Report the malaria status.
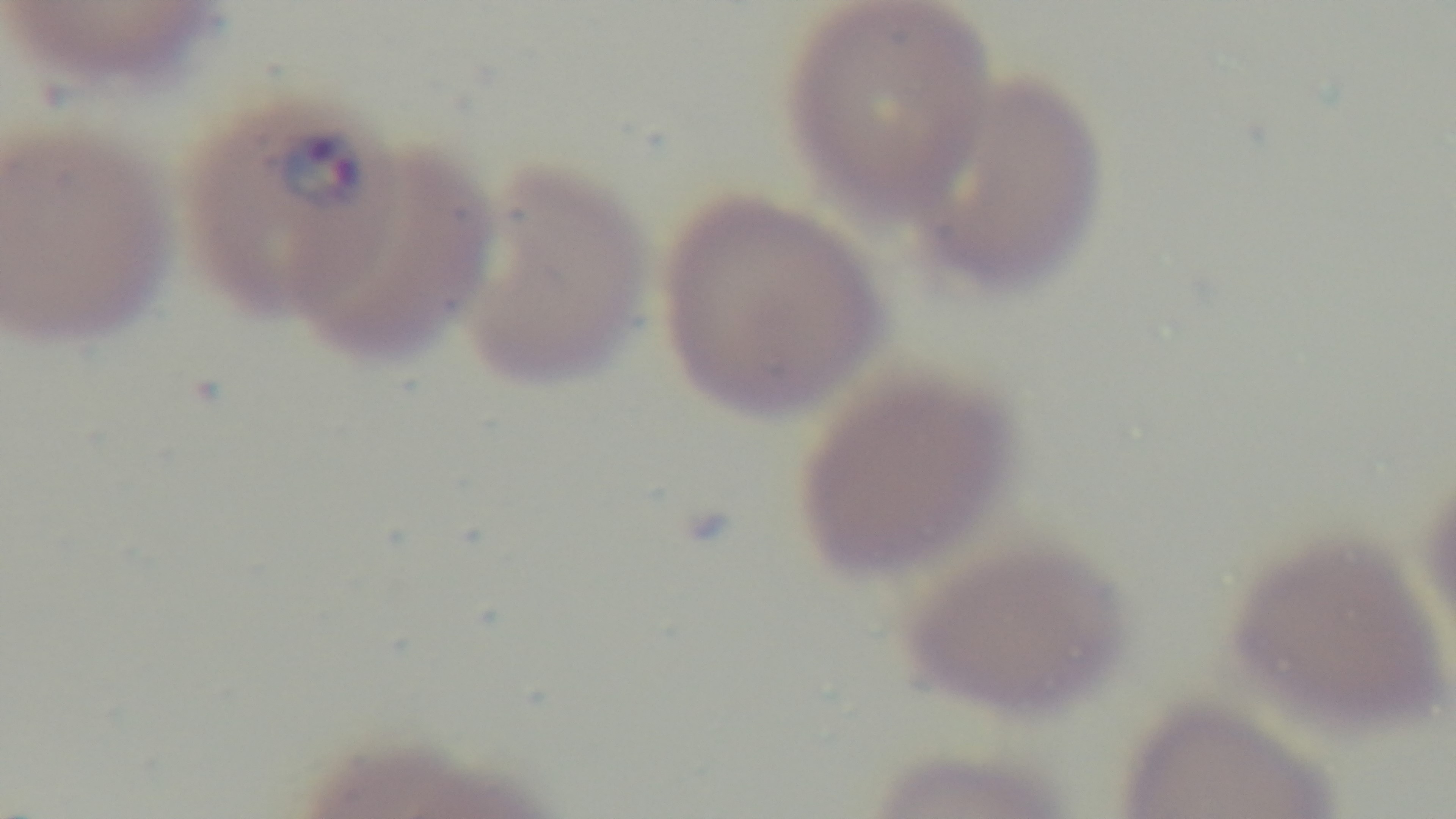

Infected.

capture = mounted 4K digital camera
preparation = thin smear
stain = Giemsa
modality = light microscopy
field of view = single
objective = 100x oil immersion